Report the malaria status of this cell.
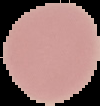

Uninfected.

preparation = thin blood smear
image type = segmented cell region with the area outside set to black
image size = 100×106 pixels